Describe the morphology of the red blood cells.
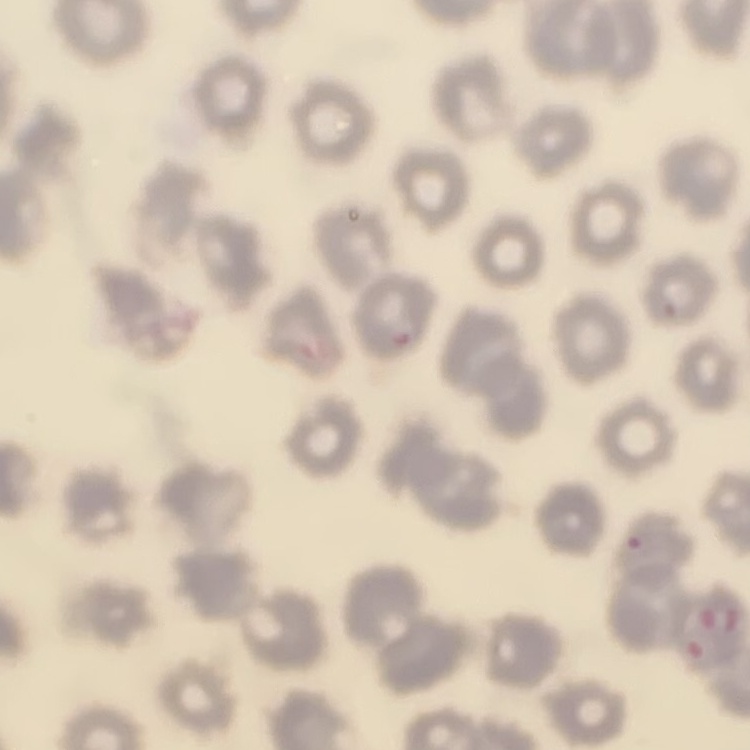

They show no rouleaux formation.

Summary:
  - Image type: square crop of a larger photomicrograph
  - Stain: Field's or Giemsa
  - Preparation: thin blood smear